Report the malaria status of this cell.
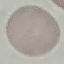

It is uninfected.

Summary:
  - Preparation: thin blood film
  - Capture: smartphone camera at the microscope eyepiece
  - Image type: automatically extracted cell patch, resized to 64 × 64 pixels
  - Stain: Giemsa